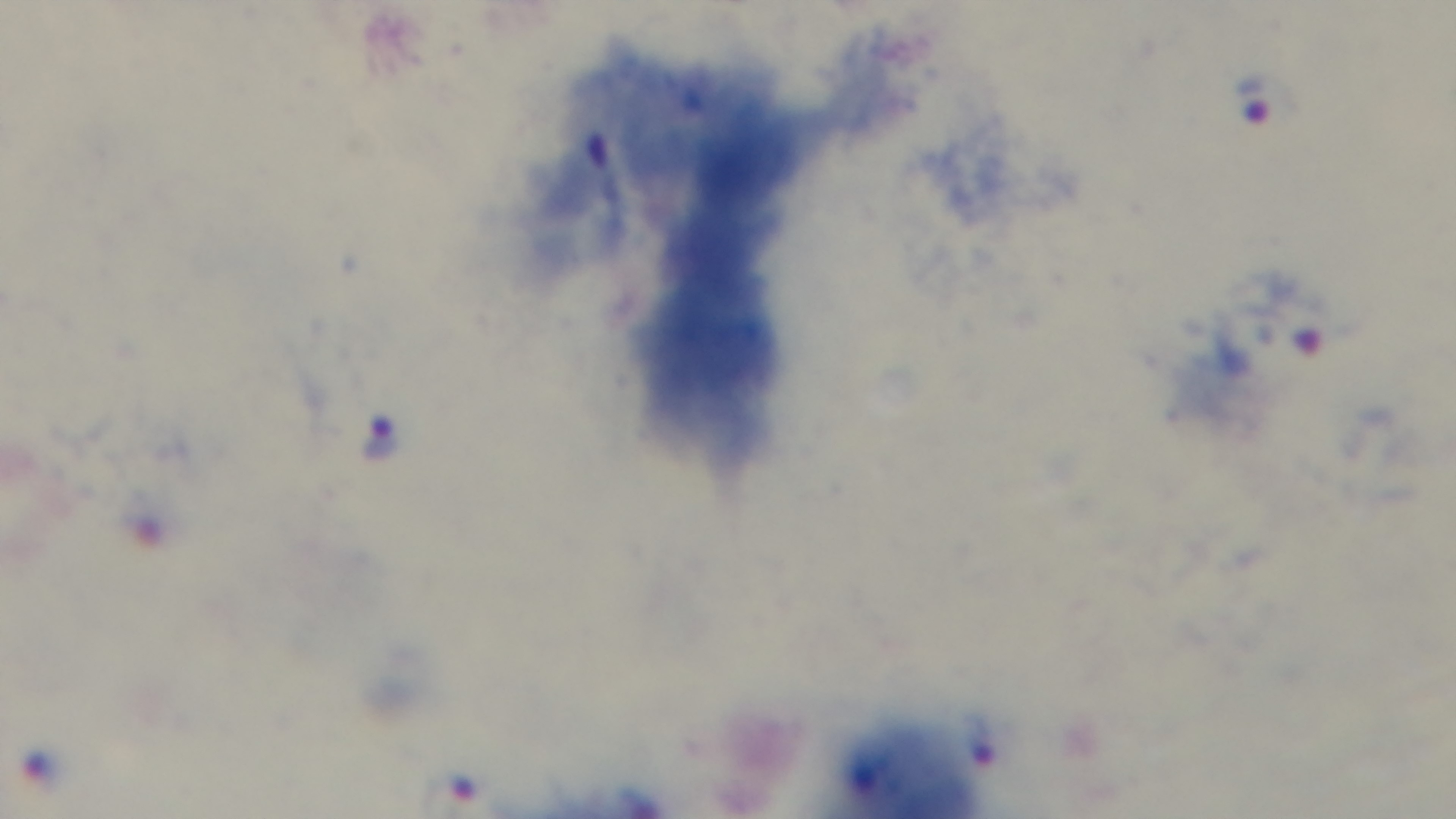
Summary:
  - Modality: light microscopy
  - Malaria status: positive
  - Capture: mounted 4K digital camera
  - Field of view: one from the slide
  - Preparation: thick blood film
  - Stain: Giemsa
  - Objective: 100x oil immersion